Identify the parasite.
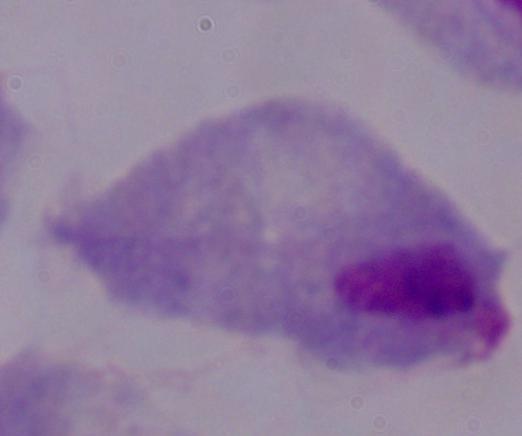
A trichomonad.

Summary:
  - Magnification: 1000x
  - Modality: micrograph